Locate every uninfected red blood cell.
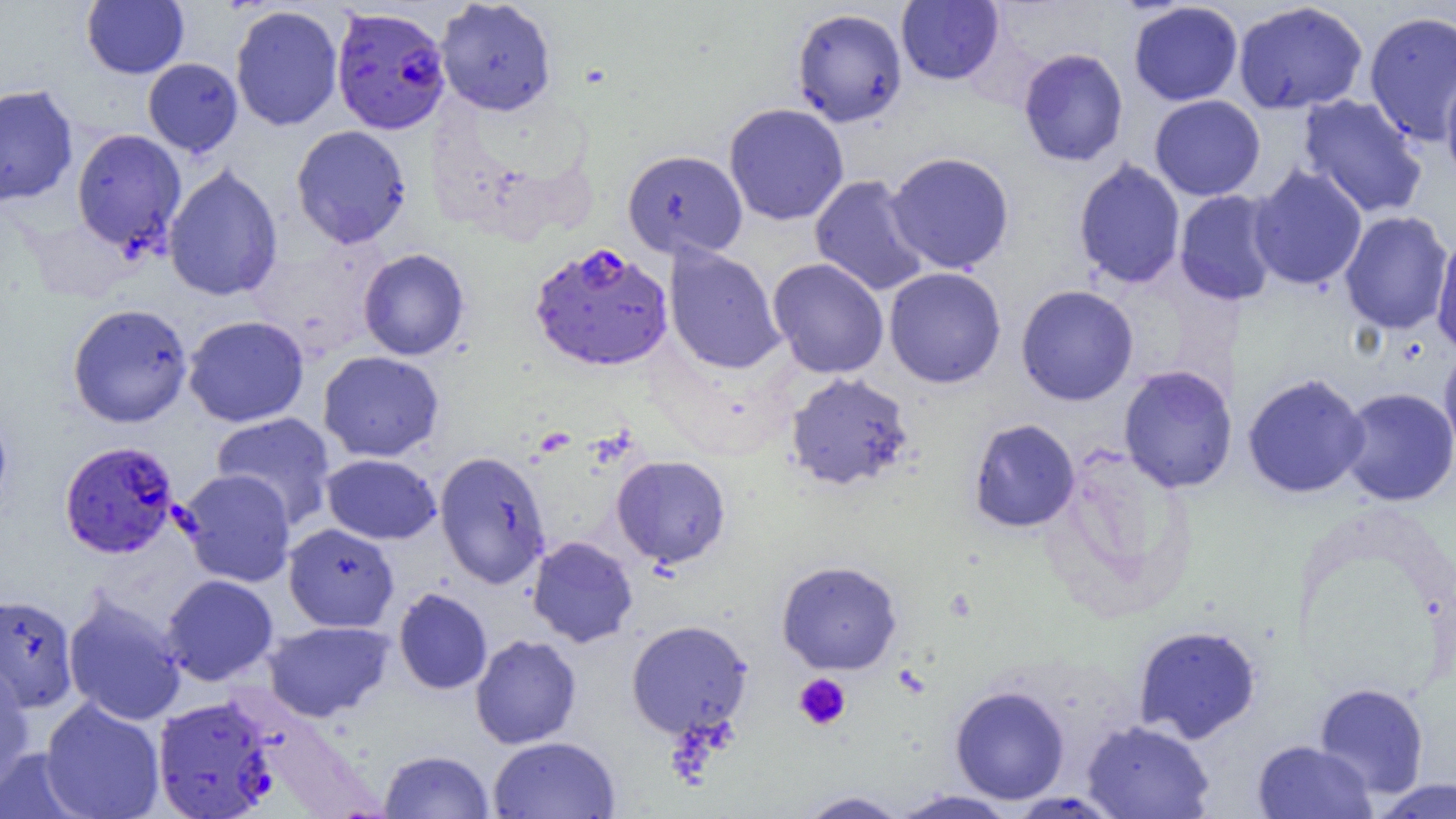
Approximate bounding boxes as (x1, y1, x2, y2) in pixels.
Uninfected red blood cells: (81, 0, 189, 79), (435, 0, 557, 116), (896, 0, 1004, 85), (1232, 1, 1368, 115), (1128, 2, 1244, 106), (230, 5, 343, 131), (791, 7, 907, 127), (1363, 10, 1456, 147), (1018, 48, 1129, 167), (142, 58, 243, 157), (1440, 67, 1456, 189), (0, 84, 78, 208), (1296, 94, 1428, 219), (1149, 95, 1266, 201), (723, 103, 849, 226), (291, 124, 412, 249), (71, 128, 187, 256), (622, 149, 748, 260), (885, 151, 1015, 274), (1073, 158, 1186, 290), (163, 163, 283, 302), (1248, 164, 1368, 291), (809, 175, 931, 296), (1174, 189, 1281, 306), (1339, 210, 1453, 335), (1431, 228, 1456, 356), (664, 245, 785, 374), (358, 248, 470, 360), (768, 257, 889, 378), (884, 267, 1006, 389), (1016, 284, 1139, 406), (66, 303, 193, 429), (183, 315, 309, 427), (1438, 343, 1456, 466), (318, 350, 444, 462), (1118, 365, 1238, 493), (784, 371, 914, 491), (1242, 372, 1370, 499), (1337, 387, 1456, 506), (0, 408, 13, 516), (211, 412, 336, 529), (969, 419, 1080, 533), (434, 450, 551, 589), (321, 453, 441, 545), (611, 455, 731, 567), (177, 469, 296, 587), (283, 523, 399, 632), (527, 536, 638, 647), (777, 559, 902, 675), (161, 574, 279, 686), (394, 588, 492, 694), (63, 592, 187, 726), (1, 593, 78, 714), (264, 620, 393, 722), (626, 620, 753, 738), (1132, 624, 1262, 744), (470, 634, 581, 749), (0, 661, 35, 794), (1313, 682, 1430, 798), (950, 685, 1070, 804), (40, 697, 165, 819), (1081, 719, 1215, 819), (488, 735, 620, 819), (1252, 739, 1376, 819), (0, 748, 90, 819), (379, 749, 494, 818), (1370, 778, 1456, 818), (890, 789, 1019, 818), (795, 790, 910, 818).

Platelet locations: (794, 673, 851, 731). Plasmodium falciparum-infected red blood cell locations: (331, 6, 451, 135), (529, 242, 673, 372), (59, 440, 179, 559), (152, 696, 277, 819). Slide-level diagnosis: Plasmodium falciparum. One field of a larger specimen. Optical microscopy. Image is 1456×819 pixels. Thin blood smear. Captured at 1000x magnification.